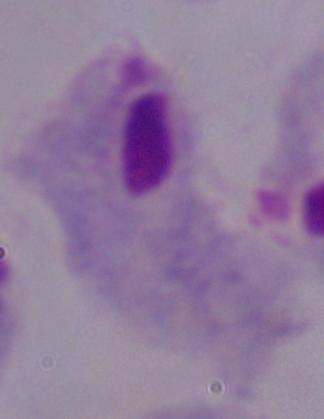
Micrograph. Captured at 1000x magnification. A trichomonad is seen.